Report the malaria status of this cell.
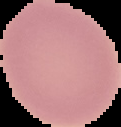
Uninfected.

{
  "image_type": "cell region segmented out of the field of view; surrounding area masked to black",
  "preparation": "thin blood film",
  "image_size": "121×127 pixels"
}